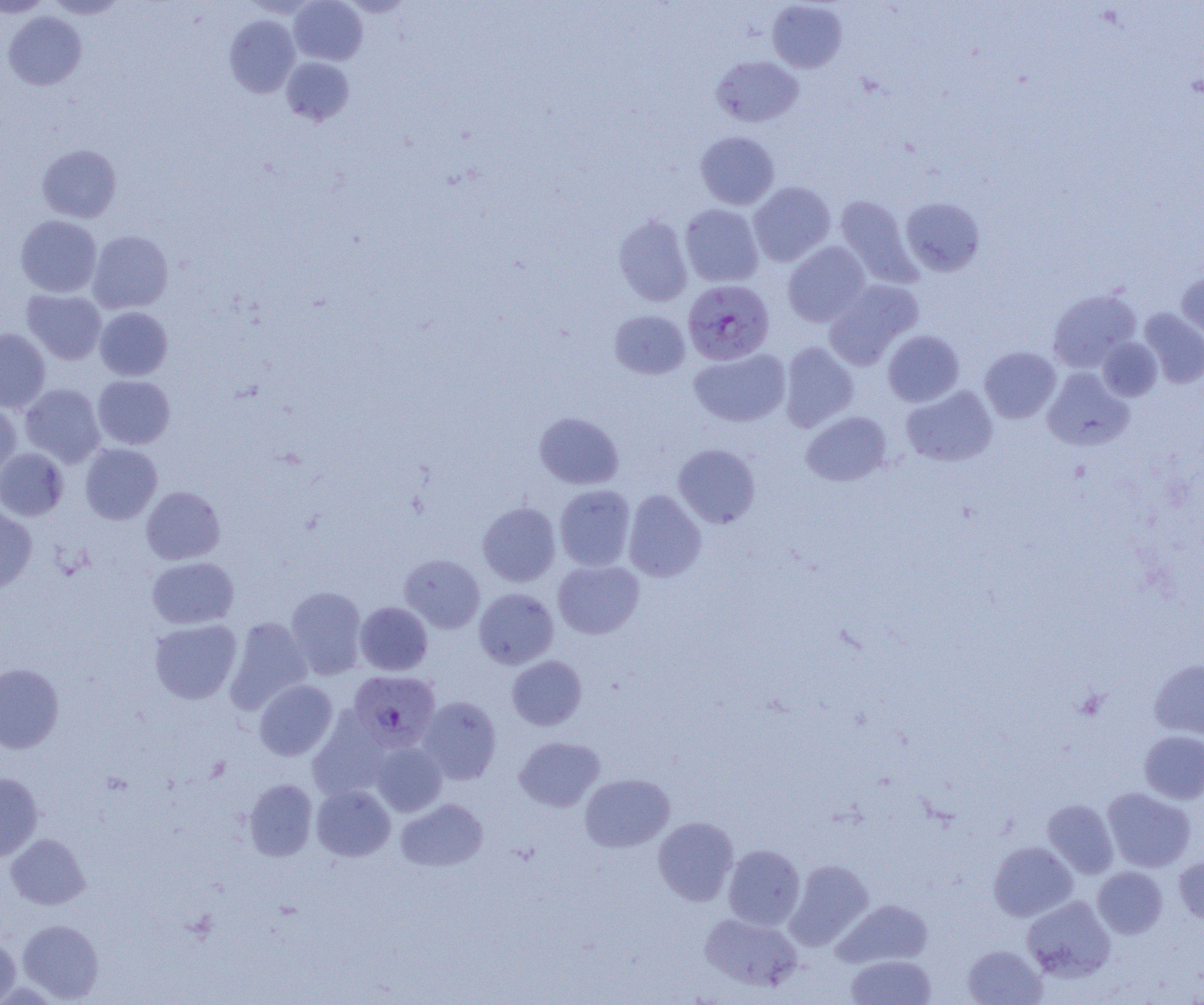

Summary:
  - Coordinate format: approximate bounding boxes as (x1, y1, x2, y2) in pixels
  - Uninfected red blood cell locations (subset): (0, 0, 51, 18), (44, 0, 129, 19), (288, 0, 367, 66), (767, 1, 847, 72), (3, 11, 86, 90), (224, 15, 300, 97), (711, 56, 803, 126), (281, 57, 354, 126), (695, 131, 779, 209), (37, 144, 122, 223), (748, 181, 835, 266), (834, 195, 919, 286), (900, 197, 985, 277), (680, 204, 764, 287), (613, 214, 693, 307), (16, 215, 102, 297), (87, 230, 173, 313), (783, 241, 870, 327), (1176, 269, 1204, 345), (824, 280, 923, 369), (22, 289, 106, 364), (1047, 289, 1141, 372), (95, 307, 173, 380), (1139, 308, 1204, 388), (609, 310, 690, 379), (0, 328, 51, 413), (883, 330, 964, 406), (1098, 337, 1162, 401), (780, 342, 858, 431), (979, 347, 1061, 423), (689, 348, 790, 427), (980, 355, 1134, 432), (1042, 367, 1133, 451), (92, 375, 176, 449), (20, 383, 106, 467), (901, 386, 998, 466), (0, 402, 22, 483), (801, 411, 892, 486), (534, 412, 624, 489), (80, 443, 162, 524), (673, 443, 761, 528), (0, 447, 68, 521), (554, 485, 636, 571), (141, 486, 225, 564), (623, 490, 706, 582), (478, 502, 560, 586), (0, 507, 37, 592), (399, 554, 485, 633), (147, 556, 239, 629), (553, 560, 644, 639), (286, 586, 368, 679), (474, 588, 558, 669), (355, 602, 433, 675), (225, 617, 312, 712), (149, 619, 242, 704), (508, 655, 586, 730), (1148, 659, 1204, 740), (0, 663, 64, 753), (254, 679, 337, 761), (418, 696, 501, 784), (309, 709, 391, 800), (1139, 730, 1204, 804), (514, 736, 605, 811), (370, 740, 447, 816), (0, 772, 43, 862), (580, 773, 675, 852), (244, 778, 317, 861), (312, 784, 395, 861), (1102, 787, 1196, 872), (396, 798, 488, 871), (1042, 800, 1119, 878), (653, 817, 739, 906), (5, 833, 90, 909), (988, 841, 1078, 922), (723, 844, 805, 930), (1174, 857, 1204, 924), (785, 859, 873, 950), (1092, 866, 1167, 939), (1022, 896, 1115, 981), (833, 898, 933, 968), (700, 913, 801, 992), (17, 919, 104, 1003), (0, 934, 20, 1004), (963, 944, 1046, 1004), (846, 954, 936, 1004)
  - Plasmodium falciparum-infected red blood cell locations (subset): (683, 279, 774, 365)
  - Slide-level diagnosis: Plasmodium falciparum
  - Magnification: 1000x
  - Field of view: single
  - Modality: optical microscopy
  - Preparation: thin blood film
  - Image size: 1204×1005 pixels